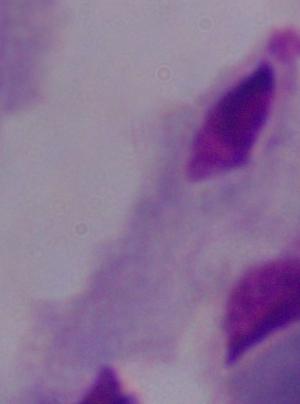
magnification = 1000x
identification = trichomonad
modality = micrograph